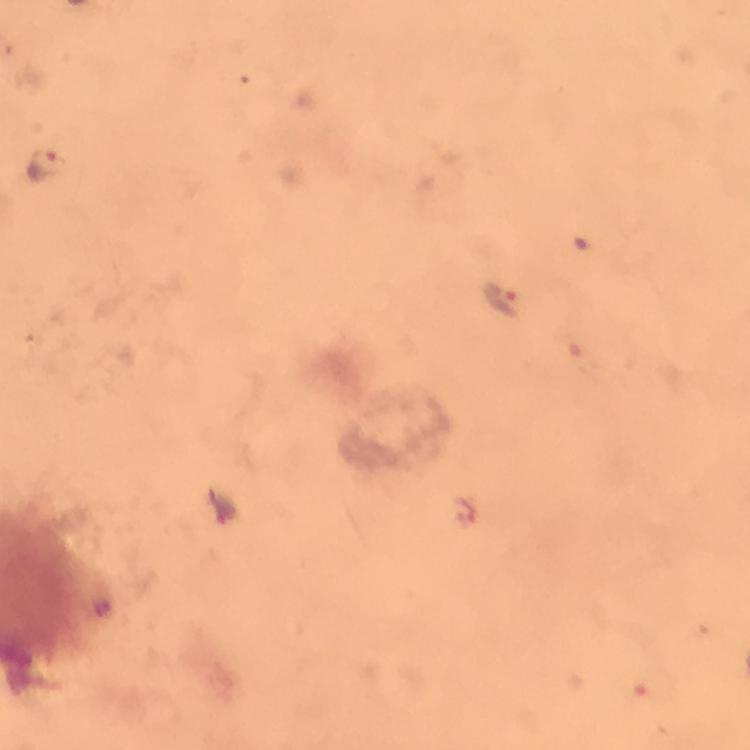
magnification: 100x
stain: Giemsa
capture: smartphone camera through the microscope
plasmodium_parasite_locations: 'approximate centers as (x, y) in pixels: (48, 169), (500, 297)'
cropped_from: a single field of view
preparation: thick blood smear
image_size: 750×750 pixels
immersion_oil: applied
context: from a malaria diagnostic workup